Classify this cell by malaria status.
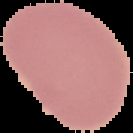
It is uninfected.

Summary:
  - Image size: 133×133 pixels
  - Preparation: thin blood smear
  - Image type: segmented cell region on a black background